Give the position of every leukocyte visible.
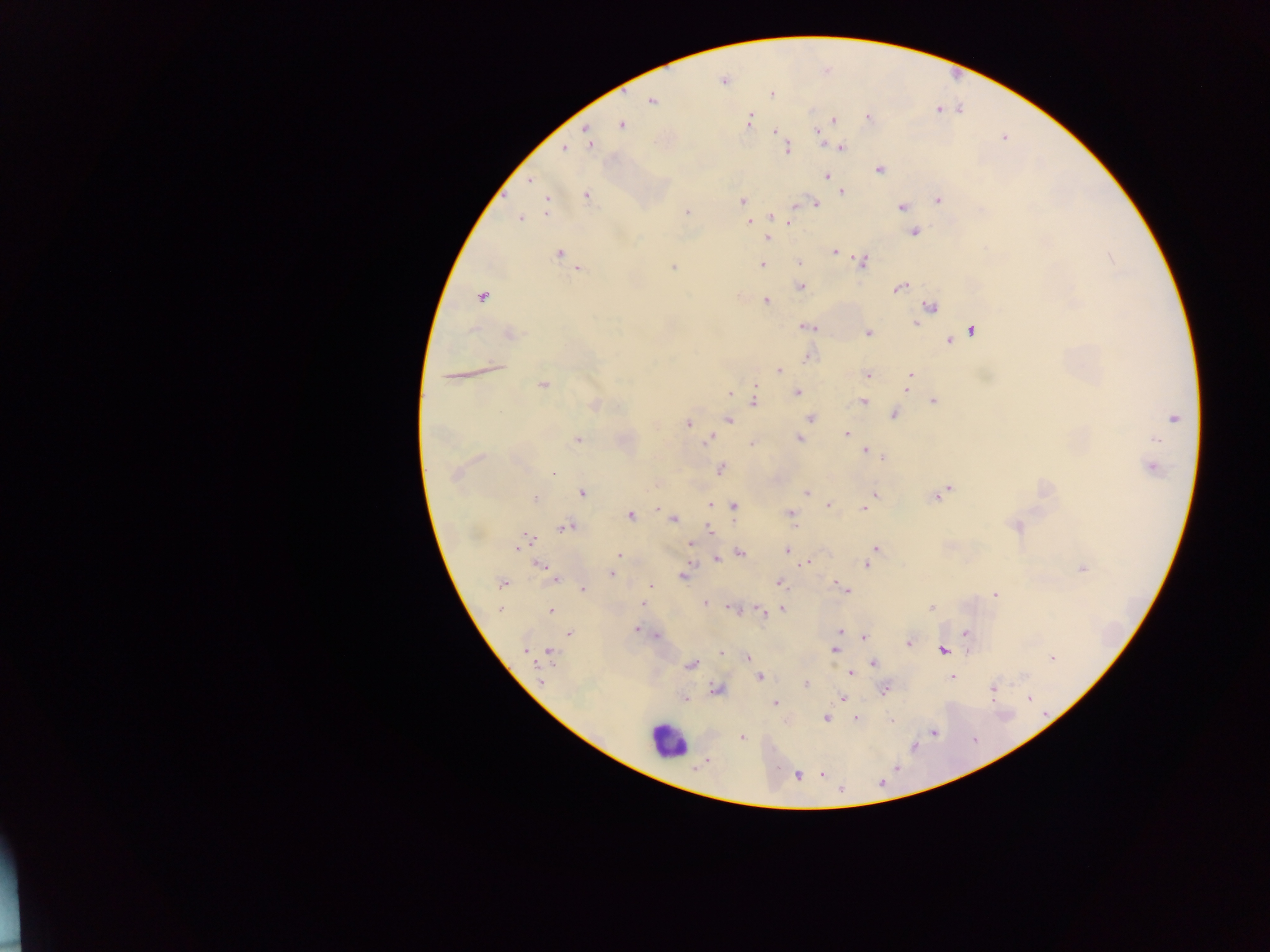
Approximate centers as x y in pixels.
Leukocytes: 667 740.

country = Ghana
capture = mobile-phone photograph through a microscope
field of view = single
image size = 1270×952 pixels
preparation = thick blood smear
Plasmodium parasite locations = approximate centers as x y in pixels: 724 81; 772 94; 652 101; 937 109; 869 117; 833 119; 748 120; 621 125; 586 131; 775 131; 819 133; 783 142; 590 144; 787 148; 841 148; 564 149; 880 169; 827 176; 530 180; 842 192; 586 194; 741 200; 939 200; 814 203; 547 204; 902 207; 686 212; 771 217; 521 219; 749 221; 790 222; 915 232; 767 239; 834 251; 559 254; 1110 257; 863 261; 800 263; 762 264; 673 268; 580 269; 801 287; 900 287; 482 296; 766 301; 931 307; 915 323; 806 327; 972 331; 868 333; 510 335; 949 341; 809 355; 779 370; 868 374; 910 375; 451 376; 909 382; 543 384; 756 385; 906 389; 798 392; 729 393; 754 401; 934 401; 863 402; 594 405; 894 415; 1173 418; 810 419; 729 420; 688 423; 846 434; 798 438; 1155 439; 578 440; 708 440; 752 444; 865 450; 883 457; 1152 468; 720 469; 553 473; 454 474; 949 487; 807 492; 582 493; 874 495; 936 497; 534 499; 710 505; 829 505; 734 506; 863 508; 658 509; 791 513; 630 516; 673 519; 1016 526; 567 527; 710 530; 527 540; 691 543; 522 544; 875 547; 787 550; 740 553; 618 555; 718 559; 808 563; 540 565; 867 565; 1083 569; 612 573; 683 577; 555 579; 780 583; 502 584; 651 585; 838 586; 583 589; 844 589; 995 595; 705 603; 644 604; 932 607; 732 608; 501 609; 783 609; 550 611; 761 611; 636 629; 840 632; 965 633; 569 634; 657 636; 864 637; 908 642; 834 650; 525 651; 550 651; 943 651; 722 652; 747 657; 1051 658; 874 663; 691 666; 850 673; 952 676; 759 677; 806 683; 717 689; 993 689; 884 690; 843 697; 684 699; 1029 699; 775 704; 827 718; 856 718; 892 720; 934 732; 742 737; 822 774; 797 775